Assess the morphology of the erythrocytes.
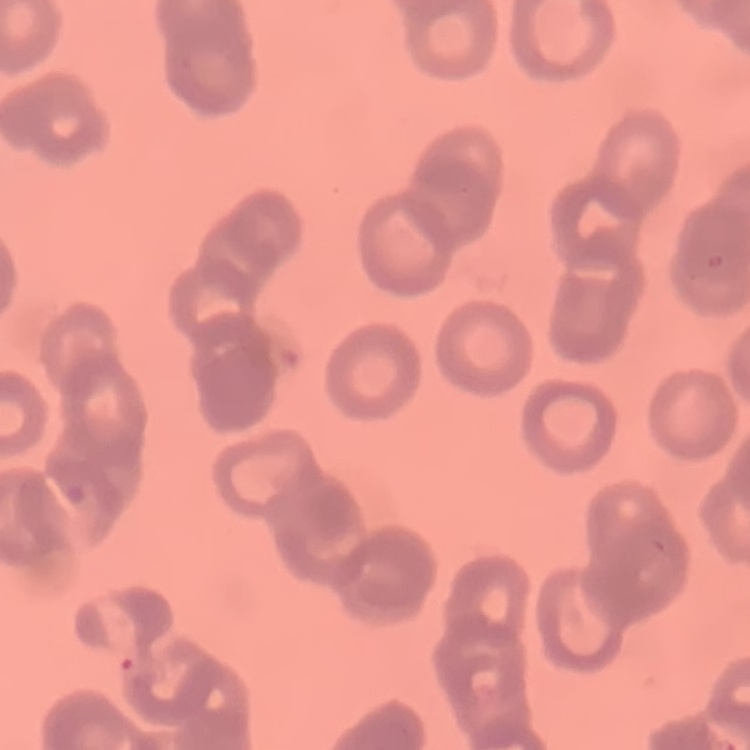

Rouleaux formation.

Summary:
  - Preparation: thin blood film
  - Image type: one tile cut from a larger photomicrograph
  - Stain: Field's or Giemsa